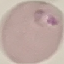
Summary:
  - Result: malaria parasites identified
  - Capture: smartphone camera at the microscope eyepiece
  - Stain: Giemsa
  - Image type: automatically extracted cell patch, resized to 64 × 64 pixels
  - Preparation: thin blood smear